Assess for parasitized red blood cells.
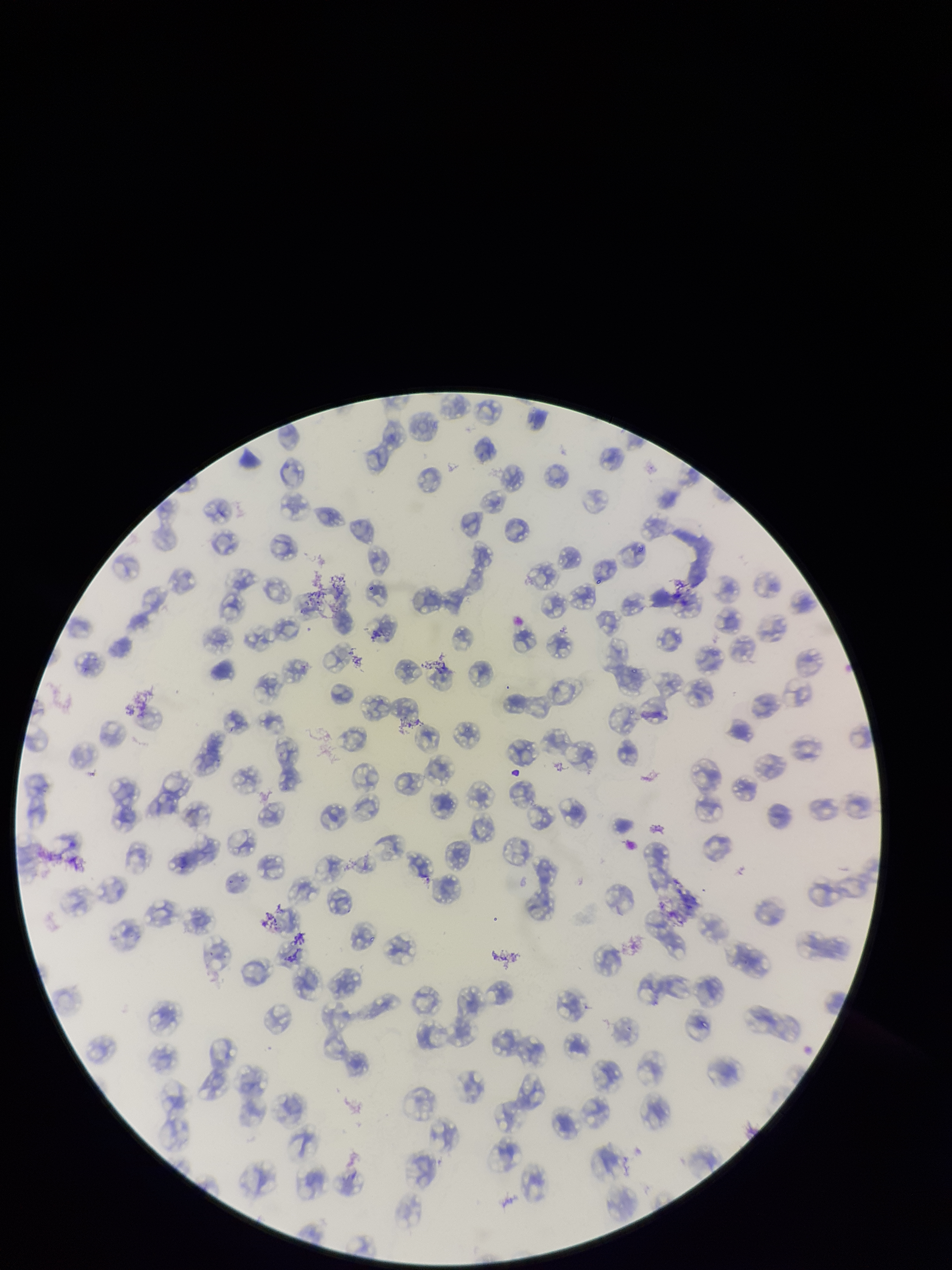

None detected.

species reported for this patient = Plasmodium falciparum
parasitized red blood cell count = 0
preparation = thin smear
stain = Giemsa
capture = smartphone photograph through the microscope eyepiece
image size = 952×1270 pixels
patient malaria status = infected
field of view = one from this slide
red blood cell count = 154